Assess the morphology of the erythrocytes.
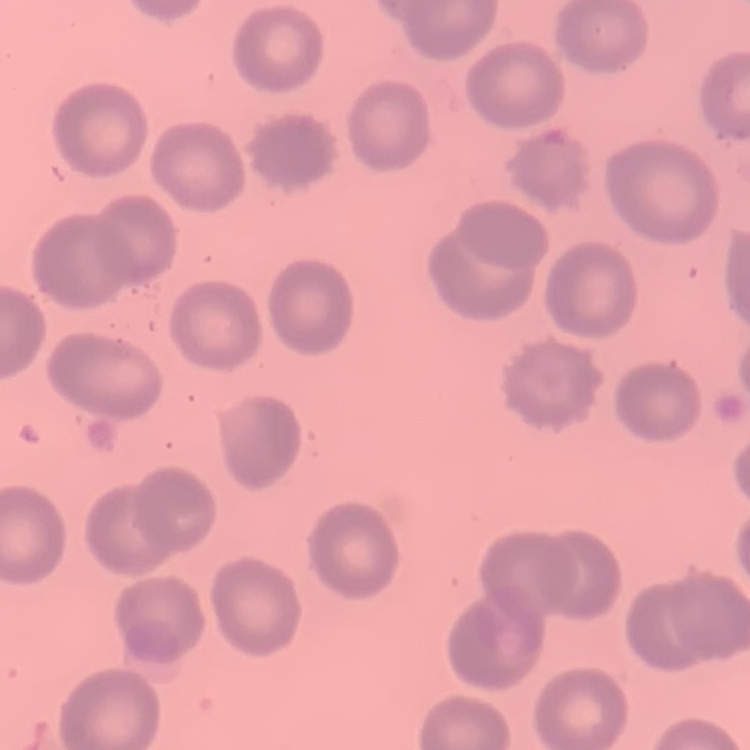
They show no rouleaux formation.

Summary:
  - Preparation: thin peripheral smear
  - Image type: square crop of a larger photomicrograph
  - Stain: Field's or Giemsa